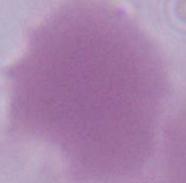
identification = erythrocyte
modality = micrograph
magnification = 1000x